Locate every uninfected red blood cell.
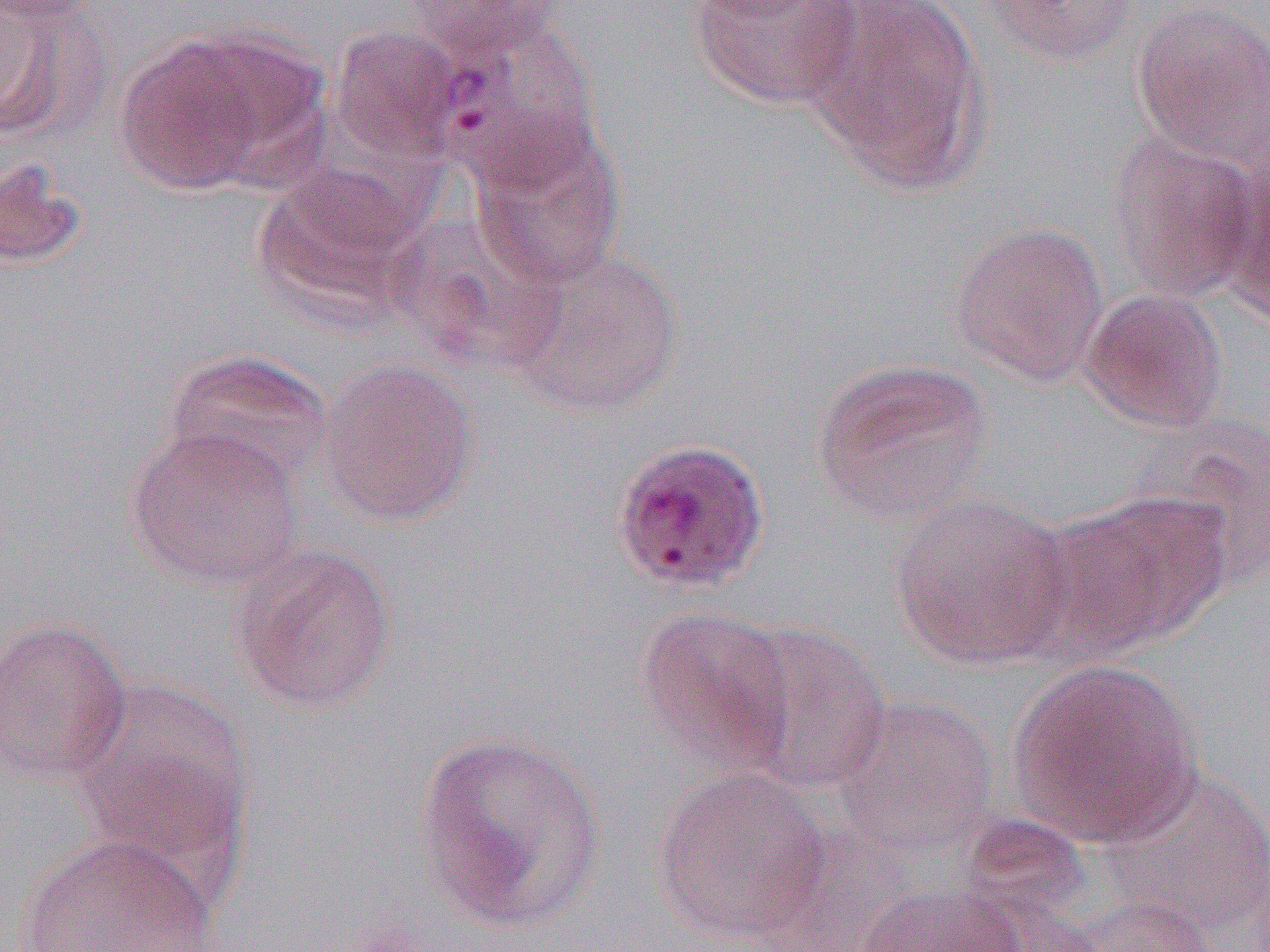

Approximate bounding boxes as [x1, y1, x2, y2] in pixels.
Uninfected red blood cells: [0, 0, 100, 142], [397, 0, 570, 57], [688, 0, 866, 111], [803, 0, 991, 193], [979, 0, 1142, 68], [0, 1, 106, 26], [1129, 1, 1270, 171], [440, 17, 607, 187], [114, 24, 323, 194], [330, 25, 470, 164], [468, 124, 626, 289], [1106, 132, 1263, 303], [0, 155, 88, 272], [1219, 160, 1269, 331], [251, 165, 422, 327], [948, 221, 1110, 389], [508, 246, 684, 420], [1079, 288, 1230, 434], [161, 348, 335, 490], [809, 356, 997, 526], [316, 357, 479, 528], [126, 423, 305, 591], [1032, 488, 1231, 661], [889, 492, 1074, 670], [228, 543, 397, 714], [634, 606, 799, 779], [0, 617, 132, 787], [729, 622, 893, 794], [1007, 659, 1204, 846], [68, 677, 256, 891], [830, 696, 1000, 856], [413, 729, 610, 935], [1101, 765, 1270, 935], [652, 766, 832, 945], [15, 833, 223, 951], [857, 883, 1030, 952], [1071, 893, 1221, 951].

slide-level diagnosis = Plasmodium vivax
field of view = one of a larger specimen
modality = light microscopy
image size = 1270×952 pixels
magnification = 1000x
preparation = thin blood film